Report the malaria status of this cell.
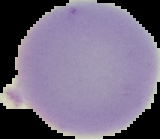

It is uninfected.

Summary:
  - Image size: 160×139 pixels
  - Image type: segmented cell region on a black background
  - Preparation: thin blood smear